Classify this cell by malaria status.
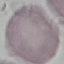

It is uninfected.

Giemsa-stained preparation. Thin blood film. Acquired by smartphone through the microscope eyepiece. Automatically extracted cell patch, resized to 64 × 64 pixels.